Report the malaria status of this cell.
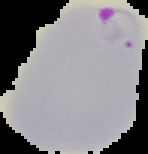

It is parasitized.

{
  "image_size": "148×154 pixels",
  "image_type": "segmented cell region on a black background",
  "preparation": "thin blood smear"
}